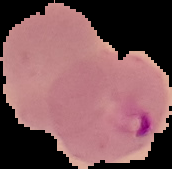
Summary:
  - Result: malaria parasites identified
  - Preparation: thin blood film
  - Image size: 172×169 pixels
  - Image type: cell region segmented out of the field of view; surrounding area masked to black